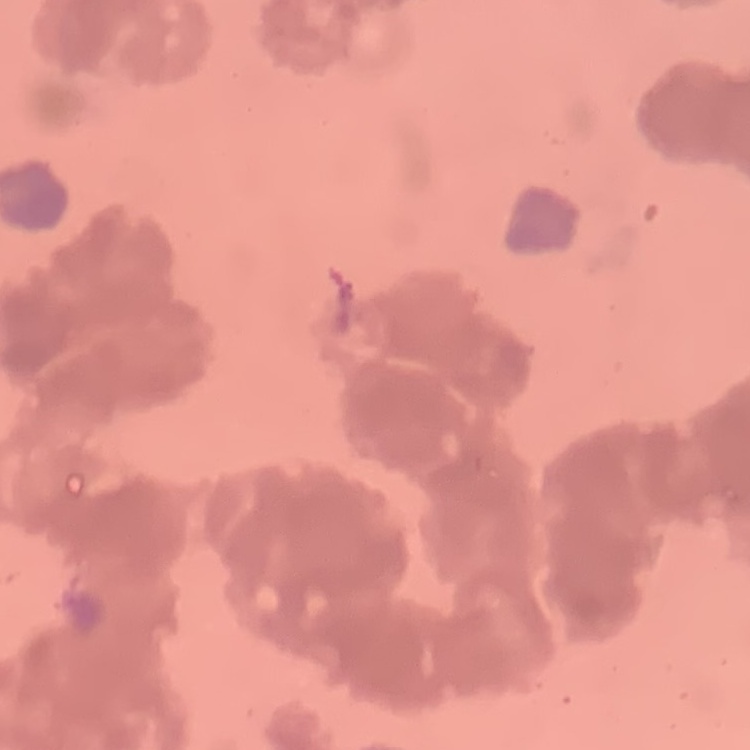
red blood cell morphology = rouleaux formation
preparation = thin blood film
stain = Field's or Giemsa
image type = square crop of a larger photomicrograph